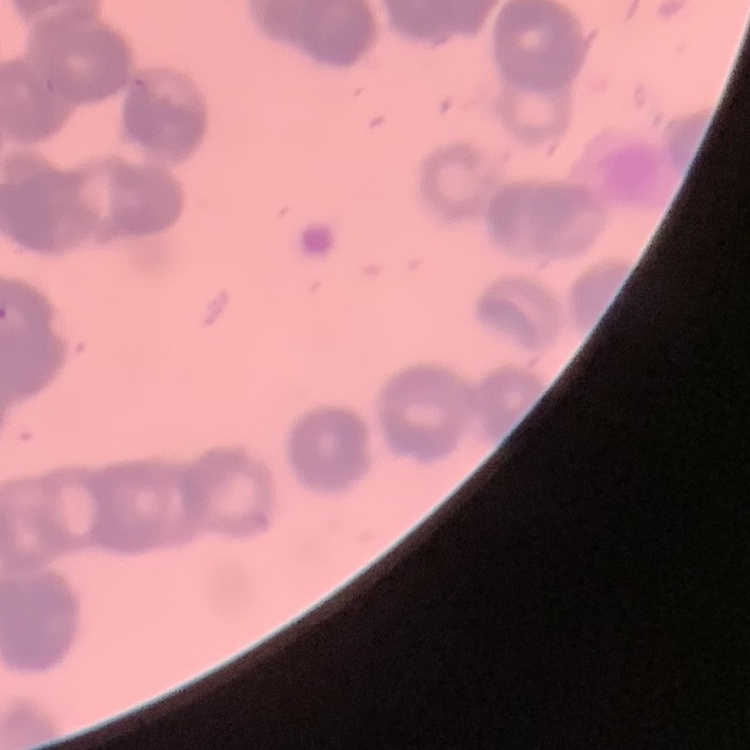 The red blood cells exhibit rouleaux formation. One tile cut from a larger photomicrograph. Stained with either Field's or Giemsa. Thin blood smear.